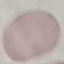

result = no malaria parasites seen
image type = automatically extracted cell patch, resized to 64 × 64 pixels
preparation = thin blood smear
stain = Giemsa
capture = smartphone through the microscope eyepiece